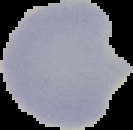

image size = 133×130 pixels
malaria status = uninfected
image type = cell region segmented out of the field of view; surrounding area masked to black
preparation = thin blood film